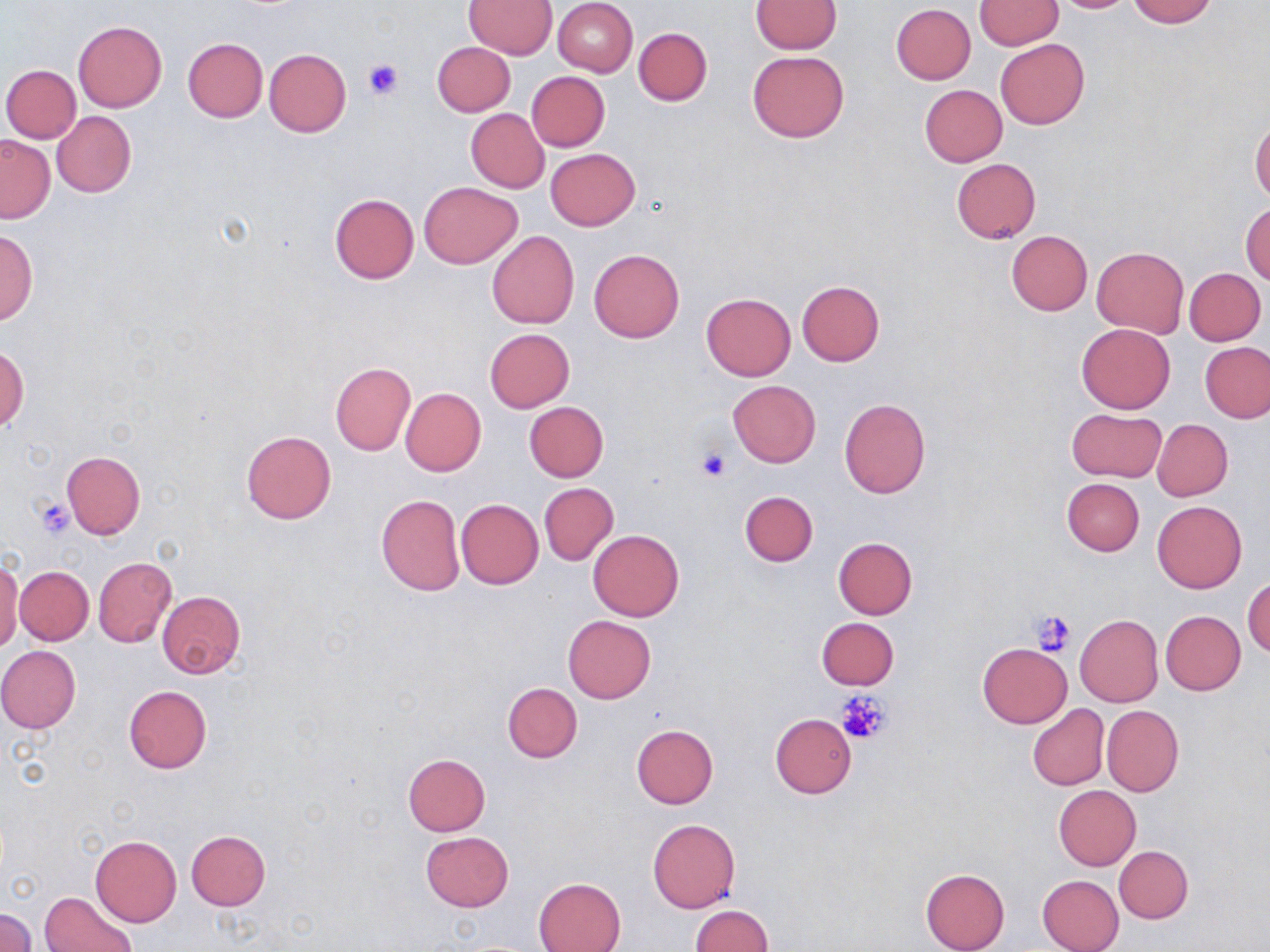
Summary:
  - Coordinate format: approximate bounding boxes as named x1/y1/x2/y2 corners in pixels
  - Platelet locations: (x1=362, y1=58, x2=404, y2=99), (x1=694, y1=447, x2=735, y2=482), (x1=35, y1=499, x2=74, y2=538), (x1=1030, y1=609, x2=1075, y2=655), (x1=837, y1=691, x2=890, y2=744)
  - Uninfected red blood cell locations: (x1=552, y1=0, x2=638, y2=76), (x1=974, y1=0, x2=1061, y2=49), (x1=1049, y1=0, x2=1136, y2=12), (x1=1128, y1=0, x2=1215, y2=26), (x1=465, y1=1, x2=557, y2=58), (x1=751, y1=1, x2=842, y2=53), (x1=890, y1=4, x2=975, y2=85), (x1=74, y1=20, x2=168, y2=112), (x1=634, y1=27, x2=711, y2=106), (x1=182, y1=37, x2=268, y2=122), (x1=995, y1=39, x2=1089, y2=129), (x1=433, y1=41, x2=515, y2=116), (x1=263, y1=48, x2=351, y2=136), (x1=747, y1=50, x2=848, y2=142), (x1=2, y1=64, x2=81, y2=142), (x1=526, y1=71, x2=609, y2=151), (x1=920, y1=84, x2=1007, y2=166), (x1=466, y1=108, x2=549, y2=193), (x1=52, y1=111, x2=136, y2=198), (x1=1250, y1=118, x2=1269, y2=203), (x1=0, y1=136, x2=55, y2=223), (x1=546, y1=149, x2=640, y2=230), (x1=951, y1=158, x2=1040, y2=244), (x1=419, y1=181, x2=522, y2=269), (x1=329, y1=193, x2=419, y2=285), (x1=1242, y1=203, x2=1270, y2=286), (x1=1, y1=229, x2=38, y2=325), (x1=487, y1=231, x2=579, y2=329), (x1=1006, y1=231, x2=1092, y2=315), (x1=1091, y1=246, x2=1188, y2=338), (x1=590, y1=249, x2=684, y2=343), (x1=1185, y1=268, x2=1265, y2=345), (x1=797, y1=280, x2=884, y2=366), (x1=701, y1=292, x2=795, y2=381), (x1=1075, y1=323, x2=1175, y2=414), (x1=485, y1=328, x2=573, y2=412), (x1=1201, y1=343, x2=1270, y2=422), (x1=1, y1=346, x2=28, y2=432), (x1=330, y1=363, x2=415, y2=455), (x1=727, y1=381, x2=820, y2=468), (x1=400, y1=387, x2=486, y2=477), (x1=839, y1=397, x2=932, y2=499), (x1=524, y1=401, x2=609, y2=482), (x1=1067, y1=408, x2=1167, y2=482), (x1=1153, y1=419, x2=1233, y2=501), (x1=241, y1=430, x2=336, y2=524), (x1=61, y1=450, x2=145, y2=539), (x1=1061, y1=477, x2=1145, y2=556), (x1=540, y1=483, x2=618, y2=565), (x1=739, y1=491, x2=818, y2=566), (x1=376, y1=493, x2=466, y2=596), (x1=456, y1=498, x2=543, y2=589), (x1=1152, y1=500, x2=1247, y2=592), (x1=589, y1=529, x2=684, y2=621), (x1=832, y1=537, x2=918, y2=619), (x1=93, y1=558, x2=176, y2=646), (x1=1, y1=561, x2=22, y2=653), (x1=14, y1=566, x2=94, y2=645), (x1=1243, y1=576, x2=1270, y2=657), (x1=156, y1=591, x2=245, y2=679), (x1=1161, y1=611, x2=1245, y2=694), (x1=563, y1=615, x2=655, y2=703), (x1=1076, y1=615, x2=1162, y2=706), (x1=817, y1=618, x2=899, y2=690), (x1=977, y1=642, x2=1072, y2=728), (x1=0, y1=646, x2=81, y2=733), (x1=503, y1=682, x2=583, y2=762), (x1=124, y1=686, x2=212, y2=773), (x1=1026, y1=704, x2=1109, y2=791), (x1=1102, y1=705, x2=1184, y2=797), (x1=770, y1=714, x2=857, y2=799), (x1=632, y1=724, x2=718, y2=808), (x1=403, y1=754, x2=489, y2=836), (x1=1054, y1=785, x2=1141, y2=870), (x1=647, y1=818, x2=741, y2=914), (x1=185, y1=829, x2=270, y2=910), (x1=419, y1=831, x2=513, y2=911), (x1=91, y1=835, x2=181, y2=926), (x1=1114, y1=845, x2=1193, y2=923), (x1=920, y1=868, x2=1010, y2=952), (x1=1037, y1=875, x2=1125, y2=952), (x1=534, y1=877, x2=626, y2=952), (x1=40, y1=891, x2=137, y2=952), (x1=691, y1=905, x2=774, y2=952), (x1=0, y1=909, x2=37, y2=951)
  - Slide-level diagnosis: negative for blood parasites
  - Preparation: thin blood film
  - Stain: May-Grünwald-Giemsa
  - Field of view: one of a larger specimen
  - Magnification: 1000x
  - Image size: 1270×952 pixels
  - Modality: light microscopy